Classify this cell by malaria status.
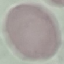

Uninfected.

Summary:
  - Preparation: thin blood smear
  - Image type: cell patch, automatically extracted from a larger field of view and resized to 64 × 64 pixels
  - Capture: smartphone camera at the microscope eyepiece
  - Stain: Giemsa